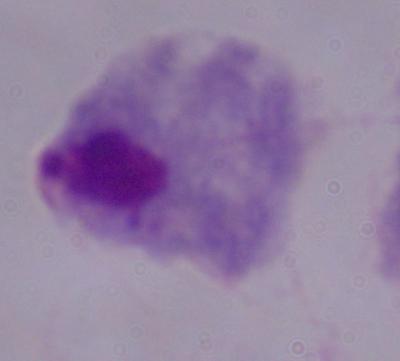
Summary:
  - Magnification: 1000x
  - Identification: trichomonad
  - Modality: photomicrograph